Assess this cell for malaria.
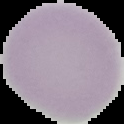

Uninfected.

preparation: thin blood smear
image_size: 124×124 pixels
image_type: segmented cell region on a black background